Name the parasite shown.
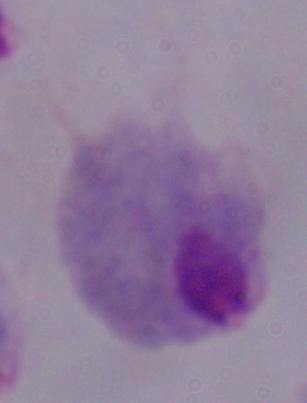

This is a trichomonad.

Micrograph. Captured at 1000x magnification.